Point out each Plasmodium parasite.
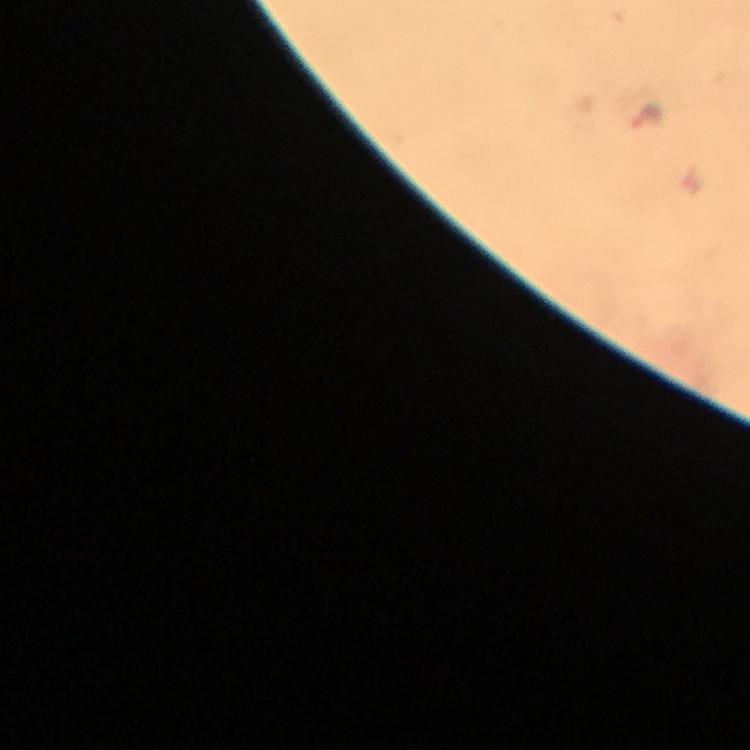
Approximate centers as (x, y) in pixels.
Plasmodium parasites: (651, 117).

capture = smartphone mounted on the microscope
image size = 750×750 pixels
cropped from = a single field of view
preparation = thick blood film
context = from a diagnostic examination for malaria
magnification = 100x
stain = Giemsa
immersion oil = applied